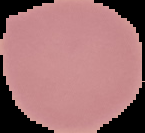 Segmented cell region on a black background. From a thin blood film. Result: no Plasmodium parasites seen. Image is 145×133 pixels.